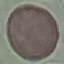

{
  "result": "no malaria parasites detected",
  "preparation": "thin smear",
  "capture": "smartphone camera at the microscope eyepiece",
  "image_type": "cell patch, automatically extracted from a larger field of view and resized to 64 × 64 pixels",
  "stain": "Giemsa"
}